Identify the parasite.
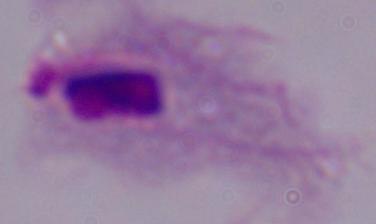

This is a trichomonad.

Summary:
  - Magnification: 1000x
  - Modality: micrograph